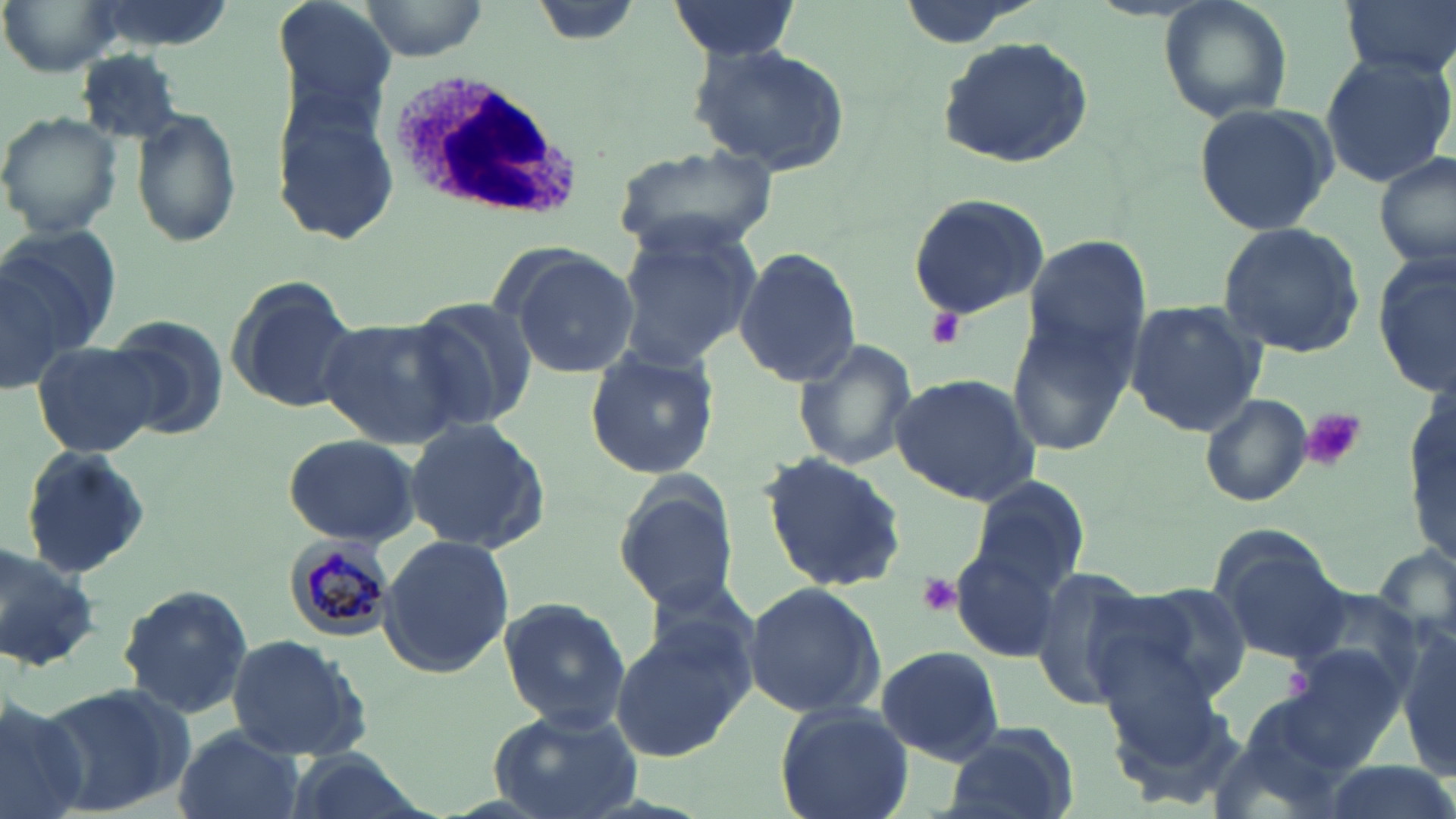
slide-level diagnosis = Plasmodium malariae
platelet locations = approximate bounding boxes as [x1, y1, x2, y2] in pixels: [926, 304, 966, 350], [1302, 407, 1365, 471], [915, 574, 963, 617], [1285, 665, 1315, 703]
preparation = thin blood film
field of view = one of a larger specimen
stain = May-Grünwald-Giemsa
uninfected red blood cell locations = approximate bounding boxes as [x1, y1, x2, y2] in pixels: [2, 0, 119, 74], [272, 0, 400, 116], [360, 0, 489, 59], [530, 0, 644, 48], [1160, 0, 1294, 122], [1339, 0, 1456, 81], [664, 1, 800, 59], [934, 37, 1098, 171], [690, 42, 852, 176], [75, 47, 186, 142], [1319, 49, 1454, 187], [269, 96, 404, 247], [1191, 101, 1337, 238], [130, 110, 243, 249], [0, 111, 123, 239], [611, 145, 779, 259], [1375, 151, 1455, 271], [905, 192, 1051, 321], [1216, 223, 1366, 359], [1, 224, 116, 372], [616, 227, 758, 369], [1021, 236, 1151, 365], [499, 245, 640, 377], [734, 246, 862, 387], [1373, 253, 1454, 398], [0, 262, 67, 396], [223, 276, 360, 413], [407, 299, 542, 431], [1123, 300, 1266, 435], [1008, 311, 1135, 453], [104, 315, 228, 439], [319, 318, 471, 448], [790, 338, 919, 472], [31, 339, 165, 459], [584, 349, 721, 478], [890, 373, 1038, 505], [1200, 392, 1312, 508], [1407, 396, 1454, 563], [402, 418, 551, 552], [281, 433, 421, 546], [19, 446, 154, 581], [761, 450, 908, 592], [613, 473, 745, 617], [965, 475, 1093, 597], [377, 533, 514, 678], [0, 536, 101, 676], [949, 536, 1070, 661], [1215, 544, 1352, 664], [1024, 566, 1151, 710], [743, 580, 883, 721], [1115, 581, 1253, 708], [118, 583, 254, 720], [498, 596, 629, 729], [610, 622, 754, 761], [1396, 630, 1456, 777], [224, 634, 372, 759], [875, 644, 1005, 765], [1283, 644, 1406, 760], [34, 681, 198, 818], [0, 690, 89, 819], [774, 702, 915, 819], [486, 708, 640, 819], [942, 723, 1079, 819], [171, 726, 303, 819], [279, 752, 434, 819], [1314, 759, 1456, 819]
white blood cell locations = approximate bounding boxes as [x1, y1, x2, y2] in pixels: [386, 70, 580, 219]
magnification = 1000x
modality = optical microscopy
image size = 1456×819 pixels
Plasmodium malariae-infected red blood cell locations = approximate bounding boxes as [x1, y1, x2, y2] in pixels: [284, 536, 395, 638]